Name the parasite shown.
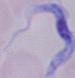

This is a trypanosome.

Captured at 1000x magnification. Photomicrograph.